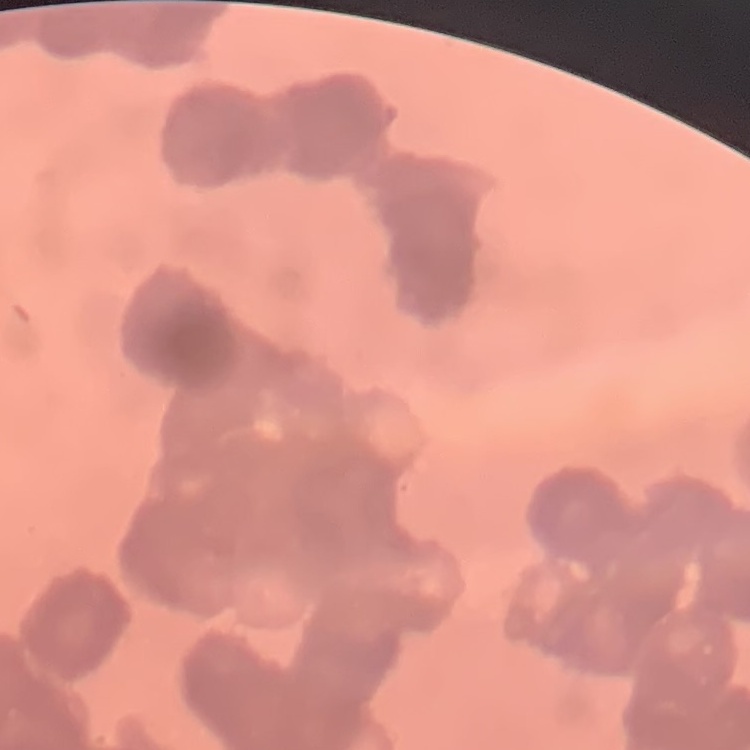

Summary:
  - Erythrocyte morphology: rouleaux formation
  - Image type: one tile cut from a larger photomicrograph
  - Preparation: thin blood smear
  - Stain: Field's or Giemsa